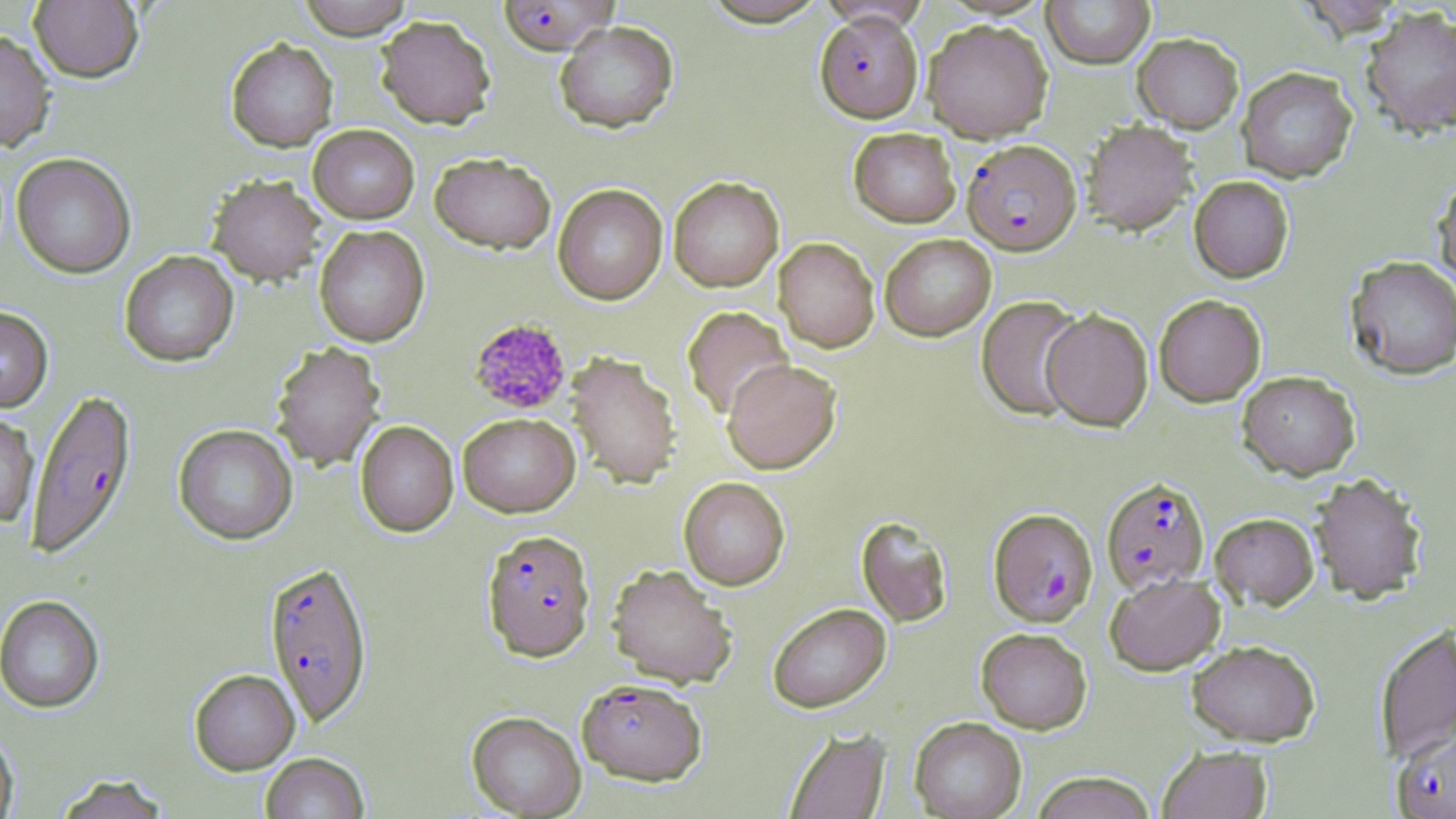
slide-level diagnosis = Plasmodium falciparum
magnification = 1000x
field of view = one of a larger specimen
modality = light microscopy
platelet locations = approximate bounding boxes as (x1,y1)-(x2,y2) corner pairs in pixels: (468,318)-(572,415)
preparation = thin blood film
image size = 1456×819 pixels
Plasmodium falciparum-infected red blood cell locations = approximate bounding boxes as (x1,y1)-(x2,y2) corner pairs in pixels: (497,0)-(619,55), (815,11)-(924,123), (962,139)-(1081,255), (25,388)-(138,562), (1101,476)-(1210,594), (988,508)-(1097,626), (482,530)-(596,662), (263,561)-(373,729), (577,679)-(706,786), (1393,726)-(1456,818)
stain = May-Grünwald-Giemsa
uninfected red blood cell locations = approximate bounding boxes as (x1,y1)-(x2,y2) corner pairs in pixels: (297,0)-(414,39), (698,0)-(833,27), (1041,0)-(1155,68), (29,1)-(143,84), (1360,6)-(1456,138), (375,15)-(496,129), (923,19)-(1053,142), (554,20)-(678,133), (0,30)-(56,153), (1133,33)-(1244,132), (226,38)-(338,152), (1236,66)-(1358,183), (1082,120)-(1197,235), (308,125)-(419,224), (848,127)-(960,228), (13,153)-(136,279), (430,153)-(556,254), (1432,172)-(1456,290), (208,175)-(326,286), (1189,175)-(1295,283), (668,176)-(784,292), (553,183)-(667,304), (314,226)-(430,347), (880,234)-(996,340), (774,237)-(879,352), (119,251)-(239,367), (1345,255)-(1456,380), (1154,294)-(1266,406), (976,295)-(1086,421), (0,306)-(53,414), (682,306)-(794,420), (1041,308)-(1153,431), (270,341)-(386,471), (566,352)-(681,489), (722,359)-(841,474), (1237,370)-(1360,479), (0,412)-(39,528), (458,412)-(580,517), (355,420)-(459,537), (173,424)-(298,545), (1309,471)-(1428,604), (678,477)-(790,590), (1210,512)-(1319,609), (856,516)-(954,628), (607,564)-(738,689), (1105,573)-(1225,675), (0,596)-(105,715), (768,603)-(891,713), (1374,625)-(1456,765), (976,627)-(1092,733), (1186,639)-(1321,746), (190,670)-(300,776), (466,712)-(586,818), (910,716)-(1027,819), (784,727)-(891,818), (0,728)-(19,819), (1157,745)-(1272,819), (261,754)-(369,819), (1029,771)-(1158,819), (55,775)-(170,819)